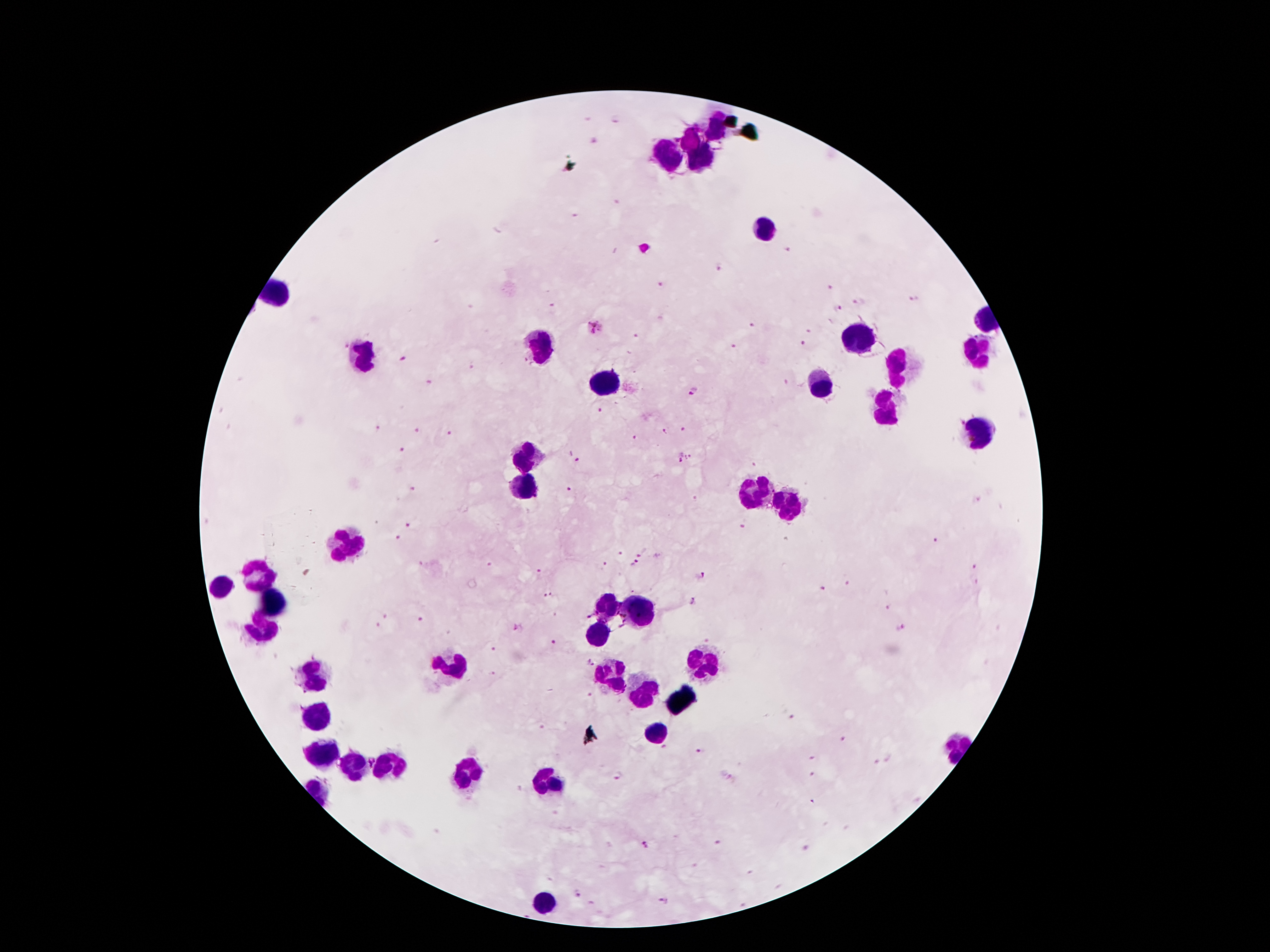
Approximate centers as (x, y) in pixels. Leukocyte locations: (716, 130), (691, 141), (667, 153), (701, 159), (763, 226), (855, 341), (540, 347), (977, 354), (363, 356), (896, 365), (607, 384), (821, 388), (885, 413), (977, 432), (526, 458), (529, 485), (752, 490), (788, 504), (342, 547), (259, 577), (219, 586), (271, 603), (604, 607), (635, 614), (262, 625), (600, 635), (699, 661), (453, 667), (613, 675), (316, 678), (644, 693), (314, 714), (658, 733), (320, 750), (355, 768), (384, 768), (471, 776), (548, 782), (543, 902). Plasmodium parasite locations: (615, 120), (595, 139), (575, 214), (789, 250), (719, 266), (661, 284), (829, 287), (914, 299), (860, 302), (838, 309), (752, 326), (596, 327), (809, 331), (637, 337), (803, 343), (734, 345), (402, 361), (474, 367), (428, 382), (786, 382), (692, 391), (599, 411), (375, 427), (683, 427), (662, 429), (415, 430), (449, 433), (633, 437), (401, 450), (679, 457), (690, 457), (577, 462), (753, 465), (415, 488), (570, 490), (694, 499), (977, 500), (408, 525), (744, 526), (397, 538), (937, 541), (643, 552), (621, 555), (635, 563), (421, 564), (606, 565), (971, 566), (541, 574), (702, 576), (847, 584), (825, 588), (548, 596), (693, 601), (888, 608), (385, 615), (555, 615), (420, 619), (376, 627), (518, 628), (900, 630), (555, 642), (495, 650), (590, 663), (491, 673), (792, 718), (843, 739), (664, 747), (699, 751), (814, 755), (891, 758), (877, 760), (814, 773), (618, 777), (811, 800), (718, 842), (646, 845), (805, 847), (577, 894), (664, 902). Image is 1270×952 pixels. Giemsa-stained preparation. Single field of view. Thick blood film. Photographed through the microscope eyepiece with a smartphone camera. 100x magnification. Patient malaria status: infected with Plasmodium falciparum.